Classify this cell by malaria status.
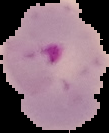

It is parasitized.

preparation: thin blood film
image_size: 109×133 pixels
image_type: cell region segmented out of the field of view; surrounding area masked to black